Point out every malaria parasite and every leukocyte.
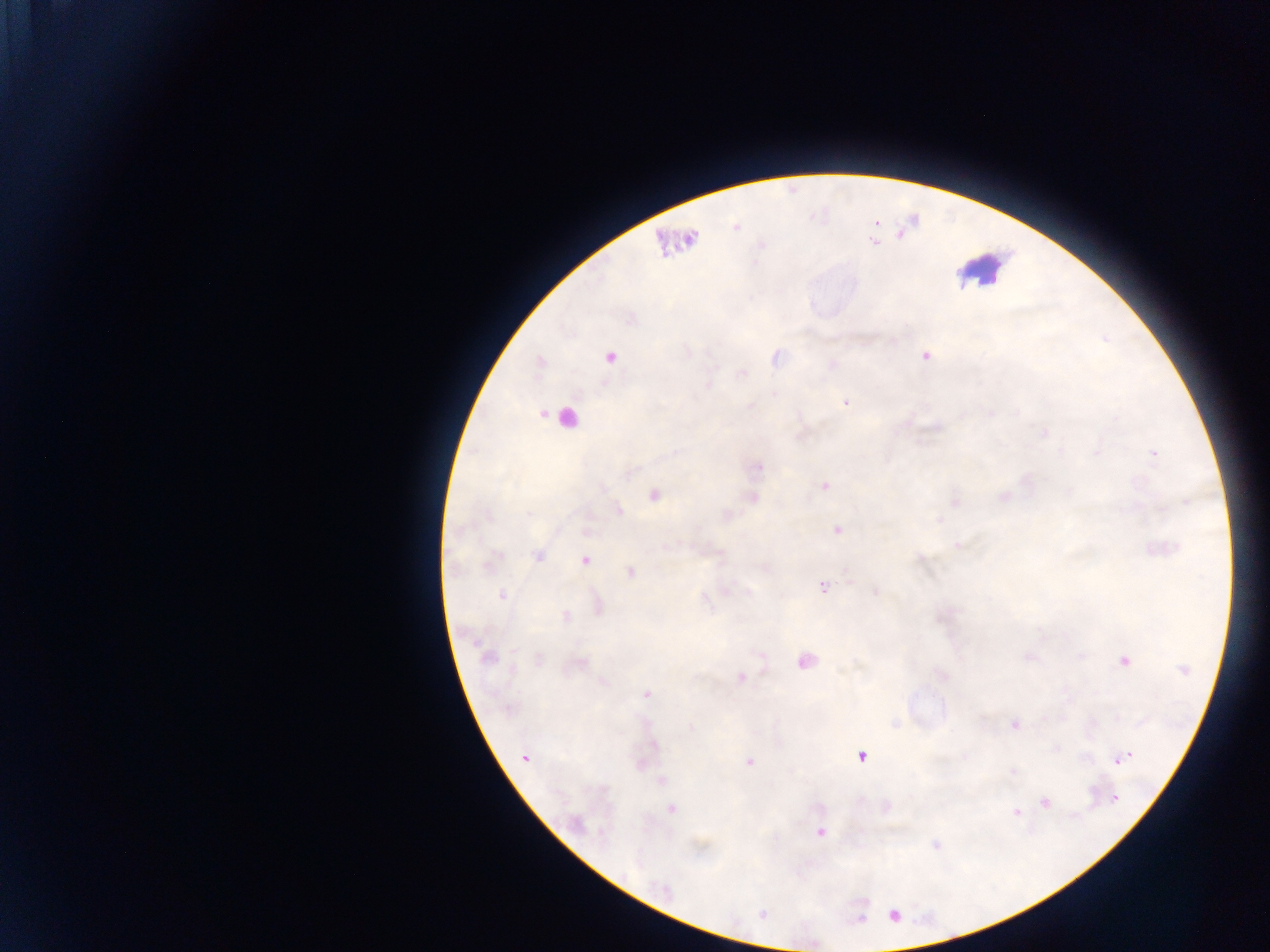

Approximate centers as [x, y] in pixels.
Malaria parasites: [736, 227], [873, 242], [627, 320], [1104, 341], [925, 355], [609, 357], [540, 363], [846, 403], [1152, 453], [824, 485], [653, 495], [1185, 502], [528, 511], [836, 529], [539, 558], [584, 561], [486, 566], [849, 583], [823, 588], [726, 590], [876, 591], [501, 596], [1128, 756], [526, 757], [862, 757], [750, 763], [1116, 799], [1016, 813], [820, 832], [935, 846], [762, 915], [894, 915], [860, 916].
Leukocytes: [975, 274].

{
  "field_of_view": "single",
  "preparation": "thick blood smear",
  "country": "Ghana",
  "image_size": "1270×952 pixels",
  "capture": "mobile-phone photograph through a microscope"
}